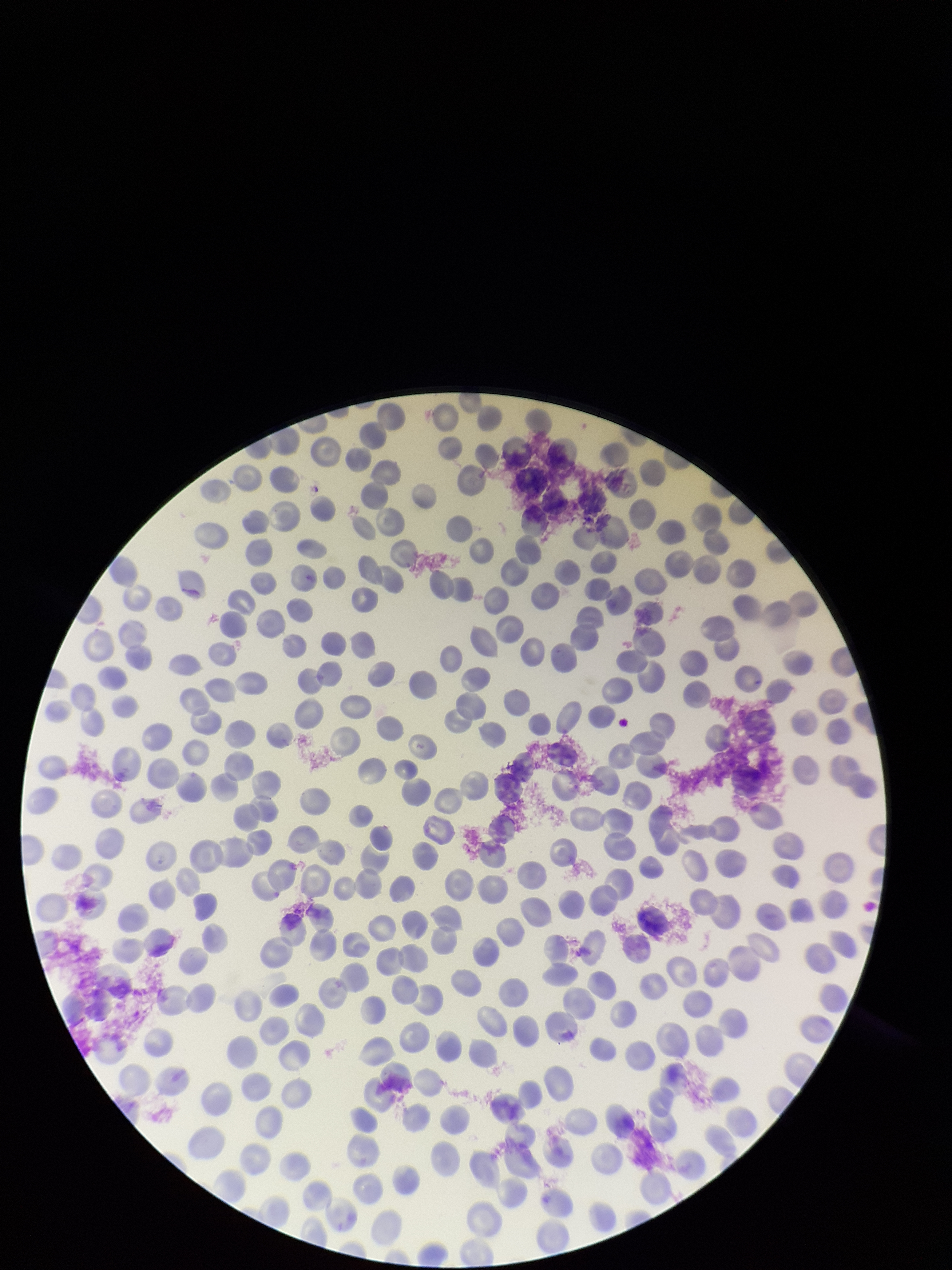
Parasitized red blood cell count: 0. Patient malaria status: infected. Parasitized red blood cells: none identified. Stained with Giemsa. Smartphone photograph taken through the eyepiece of a microscope. Image is 952×1270 pixels. Species reported for this patient: Plasmodium vivax. Red blood cell count: 281. Preparation: thin. One field from this slide.